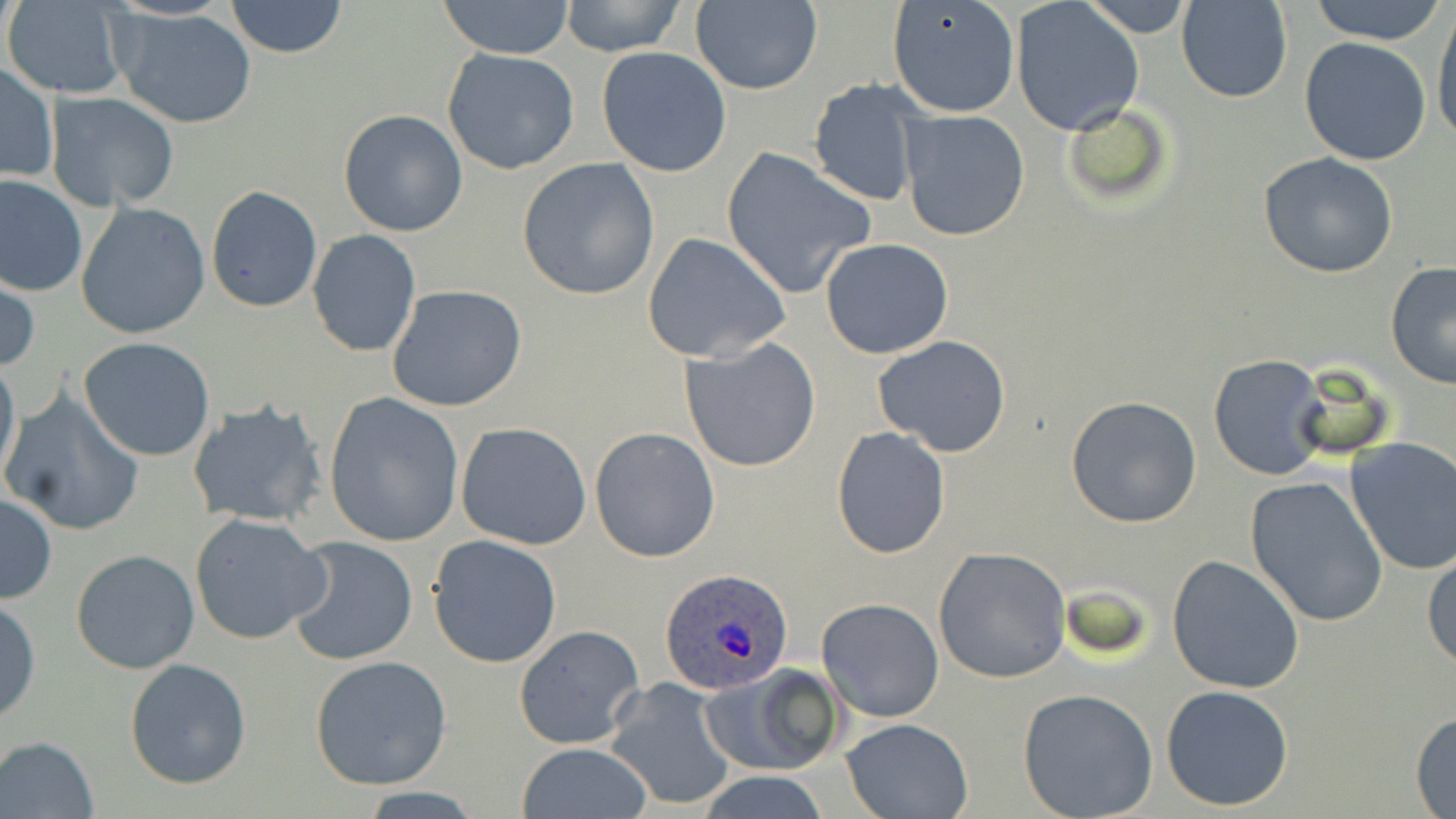

Summary:
  - Coordinate format: approximate bounding boxes as [x1, y1, x2, y2] in pixels
  - Uninfected red blood cell locations: [1176, 0, 1292, 103], [224, 1, 348, 57], [434, 1, 577, 59], [560, 1, 687, 56], [689, 1, 823, 95], [1010, 1, 1146, 135], [1084, 1, 1191, 35], [1306, 1, 1450, 45], [6, 2, 130, 98], [886, 2, 1020, 119], [1429, 3, 1456, 149], [110, 8, 258, 128], [1300, 37, 1432, 166], [595, 45, 732, 176], [441, 48, 583, 177], [0, 62, 58, 184], [808, 80, 924, 208], [46, 90, 180, 211], [1060, 100, 1175, 208], [338, 109, 468, 237], [899, 109, 1031, 242], [720, 145, 878, 299], [1257, 153, 1399, 278], [516, 158, 661, 302], [0, 175, 87, 296], [205, 186, 322, 313], [76, 202, 210, 340], [308, 228, 422, 358], [642, 232, 791, 363], [820, 238, 954, 358], [1385, 261, 1456, 390], [1, 274, 39, 376], [387, 284, 528, 413], [679, 335, 823, 471], [873, 336, 1013, 457], [77, 337, 218, 462], [0, 352, 21, 490], [1208, 355, 1327, 479], [2, 389, 146, 538], [323, 393, 465, 548], [1065, 395, 1203, 527], [187, 398, 329, 530], [455, 421, 591, 550], [589, 425, 720, 562], [830, 426, 952, 559], [1342, 438, 1456, 579], [1243, 475, 1390, 627], [0, 492, 56, 604], [189, 512, 331, 645], [428, 535, 564, 669], [286, 538, 417, 667], [932, 546, 1074, 684], [1423, 548, 1455, 671], [70, 549, 200, 675], [1166, 555, 1305, 694], [0, 597, 41, 723], [817, 598, 944, 722], [512, 624, 644, 751], [310, 655, 452, 789], [124, 659, 251, 788], [701, 664, 844, 777], [604, 677, 740, 812], [1160, 684, 1293, 812], [1017, 688, 1159, 818], [1411, 710, 1456, 815], [839, 718, 973, 819], [1, 735, 100, 817], [515, 742, 652, 819], [696, 770, 832, 819]
  - Plasmodium ovale-infected red blood cell locations: [662, 568, 793, 695]
  - Slide-level diagnosis: Plasmodium ovale
  - Magnification: 1000x
  - Preparation: thin blood smear
  - Stain: May-Grünwald-Giemsa
  - Modality: light microscopy
  - Image size: 1456×819 pixels
  - Field of view: one of a larger specimen